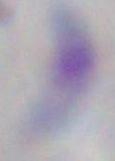 Captured at 1000x magnification. Toxoplasma gondii is shown. Photomicrograph.